Identify the blood parasite species.
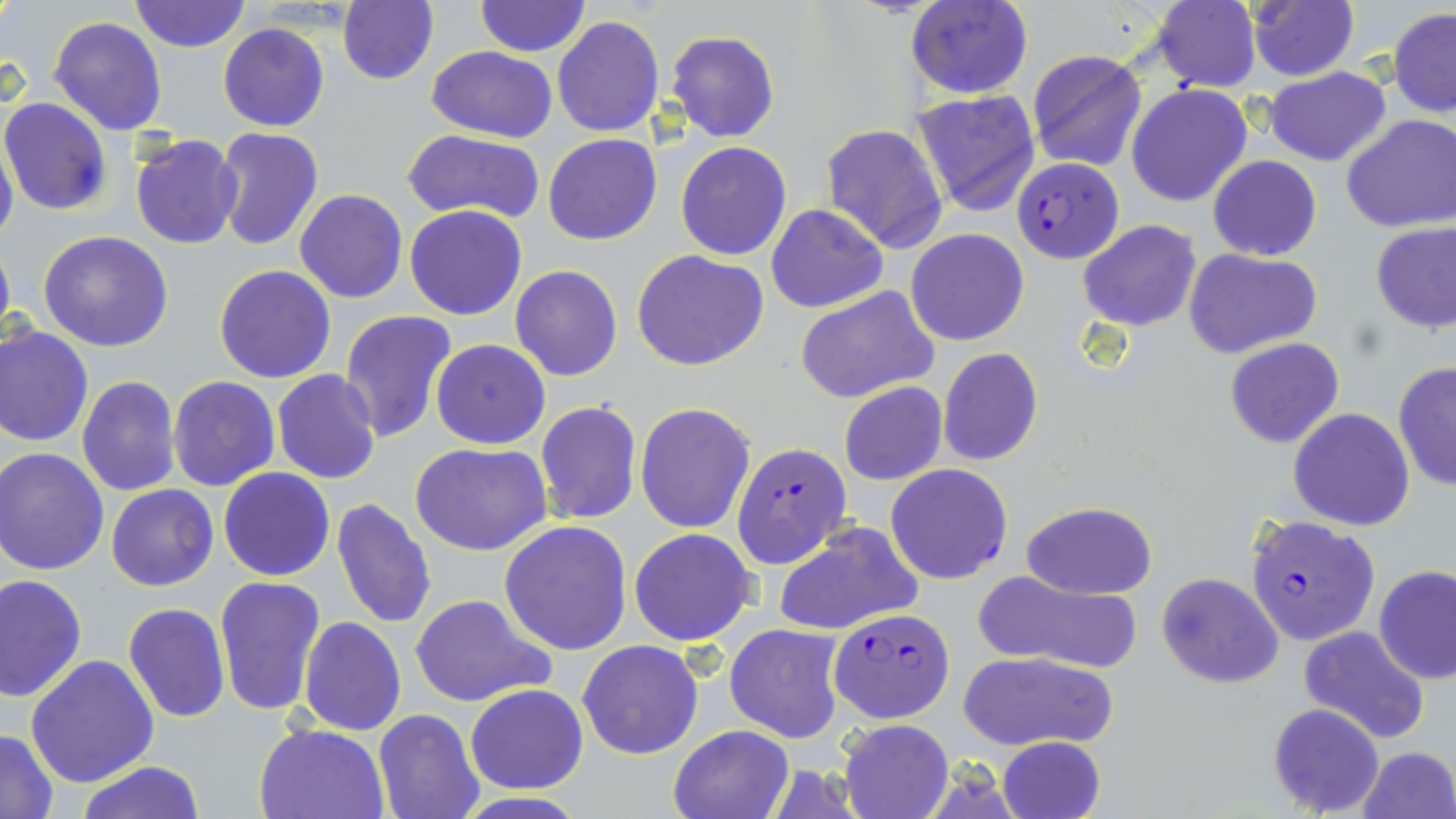
Plasmodium falciparum.

uninfected red blood cell locations = approximate bounding boxes as (x1,y1)-(x2,y2) corner pairs in pixels: (130,0)-(250,53), (337,0)-(438,86), (475,0)-(588,57), (906,0)-(1033,99), (1152,0)-(1261,91), (1246,0)-(1360,82), (1389,9)-(1456,118), (48,16)-(167,136), (552,16)-(664,138), (218,23)-(329,132), (666,31)-(780,143), (428,45)-(558,142), (1027,49)-(1146,172), (1264,67)-(1391,166), (1126,84)-(1252,207), (909,89)-(1042,217), (1,97)-(111,214), (1342,113)-(1456,233), (820,123)-(947,252), (0,127)-(18,255), (213,128)-(324,250), (403,129)-(545,225), (542,133)-(662,246), (129,135)-(244,250), (675,140)-(791,259), (1207,155)-(1322,261), (294,188)-(407,304), (766,204)-(887,313), (405,205)-(526,320), (1078,219)-(1202,332), (1370,222)-(1456,333), (906,228)-(1030,346), (38,232)-(174,352), (0,233)-(15,350), (1183,247)-(1322,358), (632,249)-(768,371), (214,264)-(338,383), (511,264)-(623,381), (795,285)-(940,405), (335,310)-(458,445), (0,323)-(94,448), (1224,338)-(1344,448), (431,339)-(550,450), (937,347)-(1043,465), (1392,362)-(1455,490), (272,369)-(382,485), (78,375)-(182,496), (168,376)-(279,491), (838,381)-(948,486), (535,400)-(642,526), (636,402)-(755,535), (1287,408)-(1414,531), (411,442)-(552,555), (2,446)-(112,576), (218,468)-(336,581), (107,483)-(219,592), (330,497)-(439,630), (1021,502)-(1157,599), (499,519)-(633,655), (772,522)-(923,636), (629,528)-(758,647), (1374,565)-(1456,685), (975,570)-(1143,672), (1156,571)-(1285,688), (214,574)-(327,717), (1,575)-(87,701), (410,593)-(554,707), (123,602)-(230,723), (298,616)-(405,736), (725,623)-(846,744), (1299,625)-(1431,745), (577,639)-(704,759), (957,651)-(1116,750), (26,654)-(159,788), (465,683)-(588,793), (1267,702)-(1385,816), (373,708)-(485,819), (839,719)-(953,819), (254,721)-(390,817), (668,723)-(795,819), (0,729)-(59,816), (998,736)-(1106,819), (1356,746)-(1455,818), (74,762)-(206,818)
preparation = thin blood film
modality = optical microscopy
image size = 1456×819 pixels
Plasmodium falciparum-infected red blood cell locations = approximate bounding boxes as (x1,y1)-(x2,y2) corner pairs in pixels: (1015,159)-(1123,263), (733,443)-(849,570), (887,464)-(1012,584), (1247,515)-(1380,646), (830,608)-(956,723)
magnification = 1000x
field of view = one of a larger specimen
stain = May-Grünwald-Giemsa